Name the parasite shown.
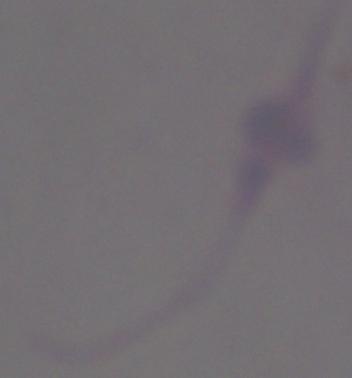
This is Leishmania.

Captured at 1000x magnification. Micrograph.